Report the malaria status of this cell.
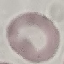

It is uninfected.

Acquired by smartphone through the microscope eyepiece. Automatically extracted cell patch, resized to 64 × 64 pixels. Thin blood smear. Giemsa-stained preparation.